State which parasite is depicted.
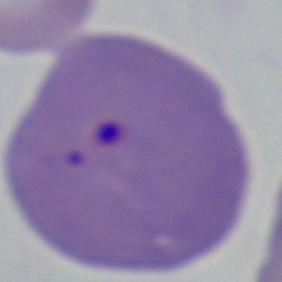

This is Babesia.

modality = micrograph
magnification = 1000x